Give the extent of all uninfected red blood cells.
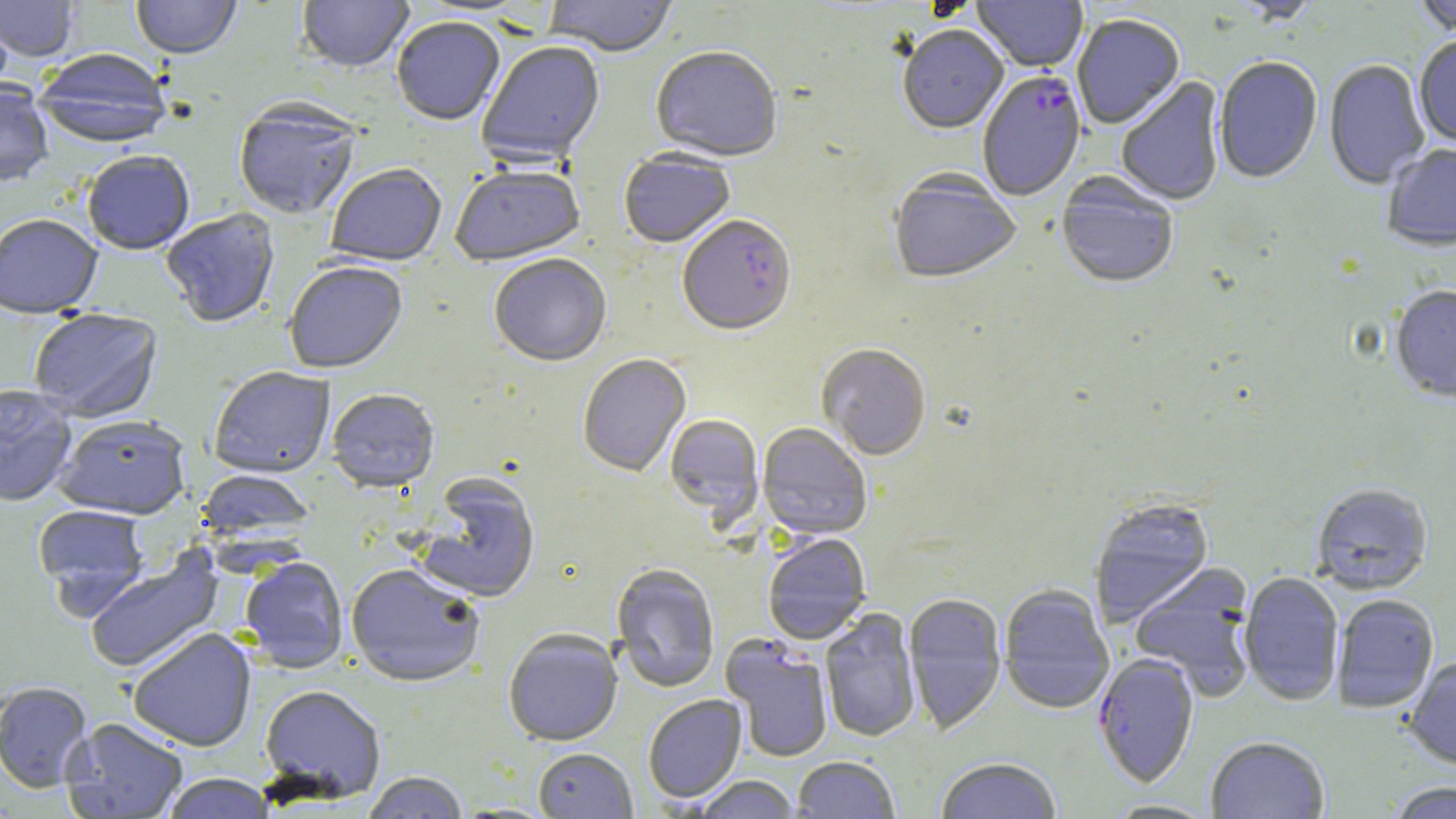

Approximate bounding boxes as [x1, y1, x2, y2] in pixels.
Uninfected red blood cells (subset): [0, 0, 80, 63], [131, 0, 241, 61], [297, 0, 414, 75], [545, 0, 677, 60], [973, 0, 1087, 73], [1229, 0, 1322, 25], [1413, 0, 1456, 39], [0, 10, 14, 98], [1072, 17, 1185, 130], [392, 19, 505, 127], [898, 28, 1009, 135], [1414, 37, 1456, 148], [478, 42, 606, 167], [651, 48, 782, 164], [32, 50, 173, 150], [1213, 58, 1322, 185], [1324, 60, 1430, 190], [1116, 78, 1226, 207], [0, 82, 53, 189], [233, 102, 361, 220], [1382, 144, 1456, 254], [82, 151, 195, 255], [619, 151, 734, 250], [326, 165, 446, 268], [450, 167, 587, 268], [889, 172, 1020, 287], [1056, 174, 1178, 291], [161, 208, 280, 329], [0, 213, 103, 318], [489, 256, 611, 368], [284, 263, 408, 375], [1390, 286, 1456, 404], [28, 309, 163, 423], [816, 346, 931, 461], [577, 354, 691, 479], [208, 368, 335, 479], [0, 385, 78, 507], [327, 390, 440, 494], [54, 414, 191, 519], [664, 415, 764, 524], [757, 424, 872, 541], [195, 470, 315, 544], [416, 474, 541, 604], [1311, 484, 1433, 595], [1089, 498, 1215, 626], [32, 504, 150, 609], [763, 534, 871, 645], [83, 550, 224, 674], [240, 558, 349, 673], [1129, 564, 1257, 701], [345, 565, 485, 689], [611, 565, 720, 693], [1239, 572, 1344, 706], [999, 585, 1114, 715], [904, 594, 1007, 735], [1332, 595, 1439, 714], [820, 608, 921, 743], [128, 627, 257, 751], [503, 631, 623, 746], [721, 636, 834, 762], [1403, 657, 1456, 771], [0, 681, 93, 792], [259, 685, 386, 803], [643, 695, 747, 803], [61, 718, 188, 818], [1206, 737, 1329, 819], [533, 748, 638, 818], [793, 756, 900, 818], [935, 758, 1062, 819], [361, 772, 469, 819], [161, 773, 275, 818], [692, 776, 800, 818], [1385, 781, 1455, 819], [1104, 800, 1219, 818].

slide-level diagnosis = Plasmodium falciparum
stain = May-Grünwald-Giemsa
preparation = thin blood smear
magnification = 1000x
modality = light microscopy
image size = 1456×819 pixels
Plasmodium falciparum-infected red blood cell locations (subset) = approximate bounding boxes as [x1, y1, x2, y2] in pixels: [978, 73, 1087, 204], [677, 217, 797, 338]
field of view = one of a larger specimen